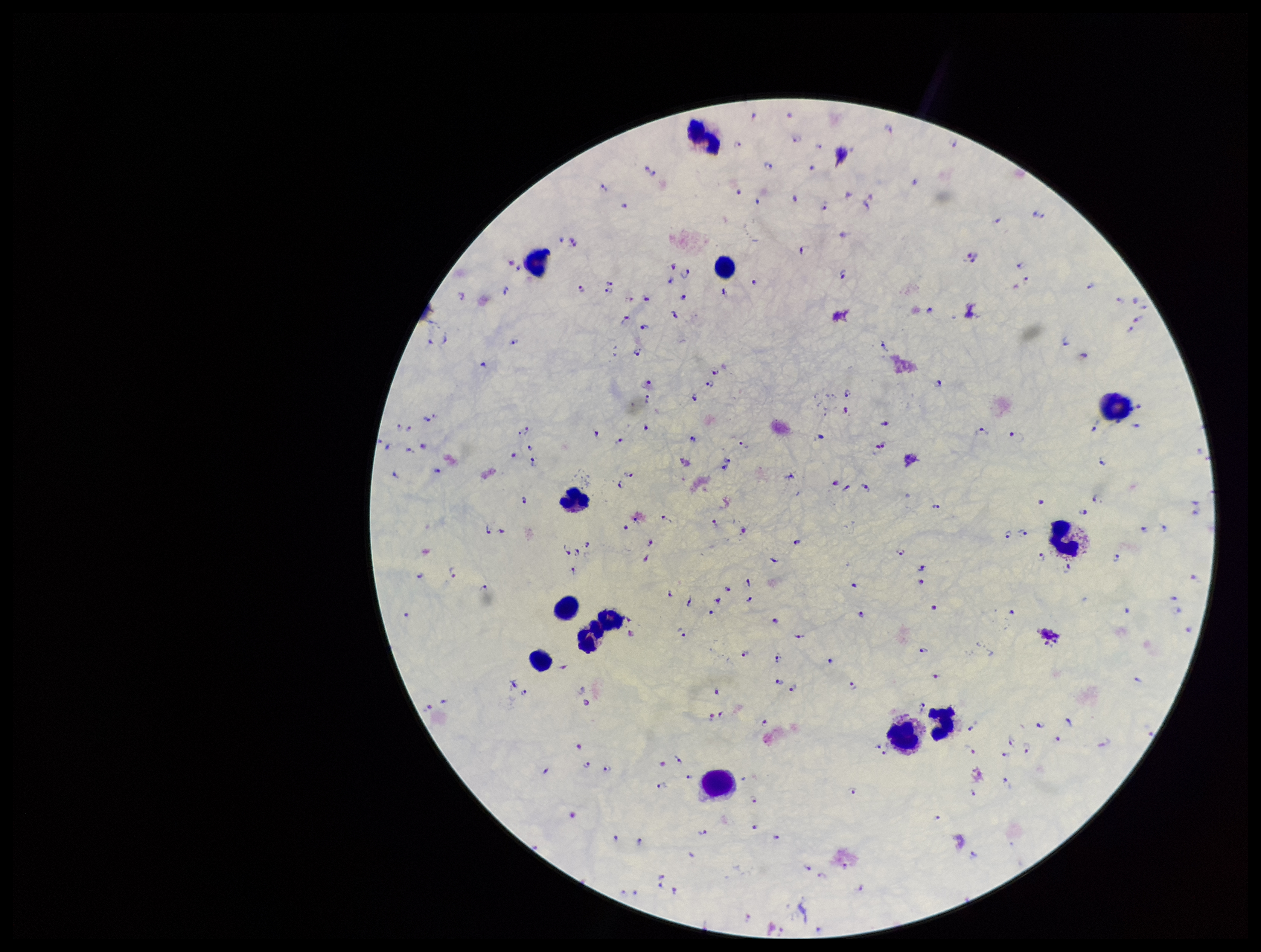
Plasmodium parasites: seen. Preparation: thick. Smartphone photograph taken through the eyepiece of a microscope. Image is 1261×952 pixels. Patient malaria status: infected. Parasite count: 190. Leukocyte count: 13. One field from this slide. Giemsa stain. Species reported for this patient: Plasmodium falciparum.